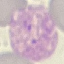
Summary:
  - Malaria status: parasitized
  - Preparation: thin blood film
  - Capture: smartphone through the microscope eyepiece
  - Stain: Giemsa
  - Image type: automatically extracted cell patch, resized to 64 × 64 pixels